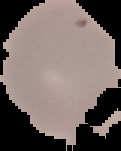
image_type: cell region segmented out of the field of view; surrounding area masked to black
malaria_status: uninfected
image_size: 121×151 pixels
preparation: thin blood film